Outline each uninfected red blood cell.
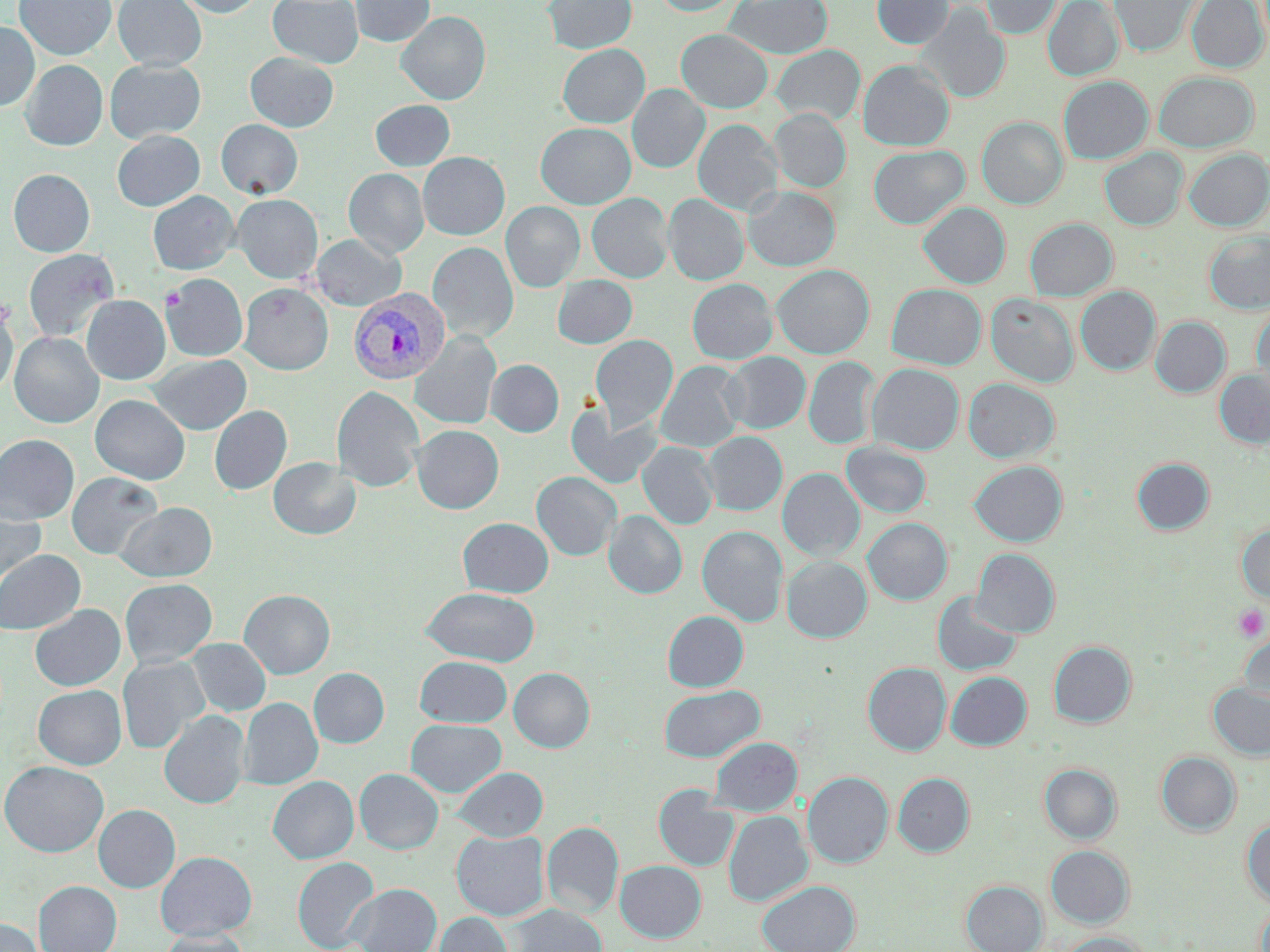
Approximate bounding boxes as [x1, y1, x2, y2] in pixels.
Uninfected red blood cells: [14, 0, 116, 60], [113, 0, 207, 71], [173, 0, 265, 17], [267, 0, 364, 68], [351, 0, 434, 46], [543, 0, 637, 54], [653, 0, 739, 15], [726, 0, 832, 59], [872, 0, 954, 48], [981, 0, 1061, 38], [1043, 0, 1123, 80], [1109, 0, 1199, 57], [1187, 0, 1268, 72], [917, 5, 1011, 103], [397, 11, 490, 105], [0, 22, 39, 111], [677, 29, 772, 112], [558, 44, 649, 127], [772, 45, 864, 125], [245, 52, 338, 132], [105, 59, 205, 143], [20, 60, 107, 151], [858, 60, 954, 150], [1154, 71, 1258, 152], [1058, 76, 1153, 164], [627, 85, 709, 172], [371, 100, 455, 170], [770, 109, 851, 192], [977, 117, 1067, 209], [217, 119, 302, 198], [693, 119, 782, 215], [536, 123, 635, 209], [112, 130, 204, 211], [868, 145, 969, 228], [1100, 148, 1187, 230], [1184, 149, 1269, 230], [418, 152, 509, 240], [344, 168, 429, 257], [8, 169, 95, 257], [744, 187, 839, 271], [148, 191, 239, 275], [587, 193, 673, 282], [232, 194, 322, 283], [664, 194, 748, 285], [501, 201, 585, 292], [918, 202, 1010, 288], [1025, 218, 1117, 301], [1203, 230, 1270, 314], [311, 234, 406, 311], [428, 242, 518, 342], [24, 248, 118, 343], [771, 264, 874, 358], [161, 274, 248, 362], [553, 275, 637, 348], [687, 278, 777, 364], [239, 283, 333, 375], [886, 283, 986, 369], [1076, 286, 1160, 375], [986, 294, 1078, 387], [82, 295, 170, 384], [1251, 305, 1270, 396], [0, 306, 17, 397], [1150, 316, 1230, 397], [411, 331, 501, 429], [10, 332, 103, 428], [591, 335, 678, 431], [721, 352, 810, 433], [147, 355, 252, 435], [804, 357, 880, 448], [486, 359, 564, 437], [656, 361, 745, 452], [867, 363, 964, 454], [1214, 369, 1270, 448], [963, 378, 1059, 463], [331, 386, 425, 492], [90, 394, 190, 485], [567, 404, 661, 488], [209, 406, 292, 495], [412, 425, 503, 514], [702, 431, 787, 515], [0, 434, 79, 524], [841, 441, 932, 518], [638, 442, 718, 529], [269, 457, 360, 539], [1132, 457, 1214, 535], [969, 460, 1067, 546], [778, 468, 864, 561], [532, 471, 621, 560], [66, 472, 163, 560], [0, 500, 46, 588], [117, 502, 217, 582], [604, 510, 687, 598], [458, 517, 553, 597], [863, 518, 952, 604], [1236, 524, 1270, 603], [697, 526, 787, 626], [971, 548, 1059, 637], [0, 549, 85, 635], [782, 556, 872, 642], [120, 578, 217, 667], [421, 587, 540, 666], [239, 589, 335, 678], [932, 591, 1022, 676], [30, 604, 125, 691], [662, 611, 748, 691], [1237, 629, 1269, 708], [186, 638, 271, 716], [1049, 641, 1136, 728], [118, 655, 209, 754], [415, 656, 512, 727], [863, 662, 951, 755], [509, 667, 594, 752], [309, 668, 389, 747], [946, 672, 1031, 750], [1208, 683, 1270, 760], [659, 684, 764, 762], [33, 685, 126, 769], [239, 698, 322, 789], [159, 710, 250, 808], [406, 719, 506, 796], [709, 737, 802, 816], [1156, 751, 1241, 836], [1, 761, 108, 856], [1040, 763, 1121, 843], [452, 767, 548, 841], [355, 769, 443, 854], [803, 772, 892, 867], [893, 773, 974, 856], [268, 776, 358, 864], [654, 787, 738, 871], [93, 804, 180, 892], [724, 811, 812, 906], [1242, 818, 1270, 906], [542, 822, 623, 916], [452, 830, 548, 920], [1045, 845, 1134, 928], [155, 851, 257, 940], [292, 857, 380, 952], [615, 860, 706, 942], [757, 880, 860, 952], [962, 880, 1047, 952], [33, 881, 122, 952], [347, 883, 442, 952], [1255, 902, 1270, 952], [509, 904, 607, 952], [432, 911, 511, 952], [0, 918, 45, 952], [158, 929, 251, 952], [1058, 933, 1152, 952].

slide_level_diagnosis: Plasmodium vivax
modality: optical microscopy
stain: May-Grünwald-Giemsa
preparation: thin blood film
image_size: 1270×952 pixels
plasmodium_vivax_infected_red_blood_cell_locations: 'approximate bounding boxes as [x1, y1, x2, y2] in pixels: [348, 288, 450, 385]'
field_of_view: single
magnification: 1000x
platelet_locations: 'approximate bounding boxes as [x1, y1, x2, y2] in pixels: [1233, 605, 1268, 641]'